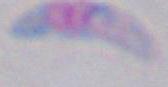

Micrograph. Toxoplasma gondii is shown. 1000x magnification.